Identify the parasite.
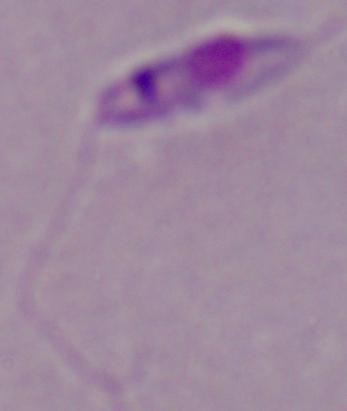
Leishmania.

Summary:
  - Modality: micrograph
  - Magnification: 1000x